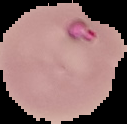
Summary:
  - Preparation: thin blood smear
  - Result: Plasmodium parasites detected
  - Image type: cell region segmented out of the field of view; surrounding area masked to black
  - Image size: 127×124 pixels